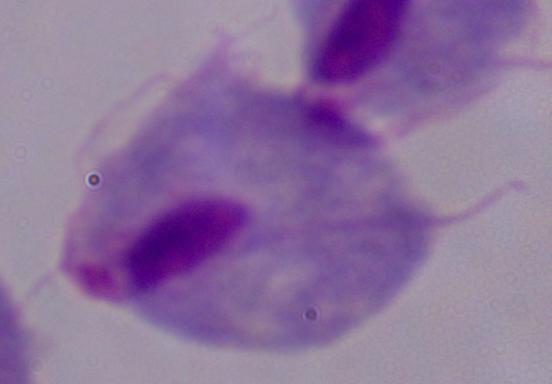

Photomicrograph. 1000x magnification. A trichomonad is shown.